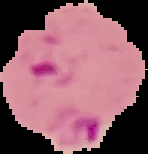

preparation: thin blood smear
malaria_status: parasitized
image_size: 148×154 pixels
image_type: segmented cell region on a black background